Report the malaria status of this cell.
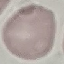
Uninfected.

Giemsa stain. Photographed with a smartphone camera at the microscope eyepiece. Thin smear of blood. Cell patch, automatically extracted from a larger field of view and resized to 64 × 64 pixels.